State the preparation type.
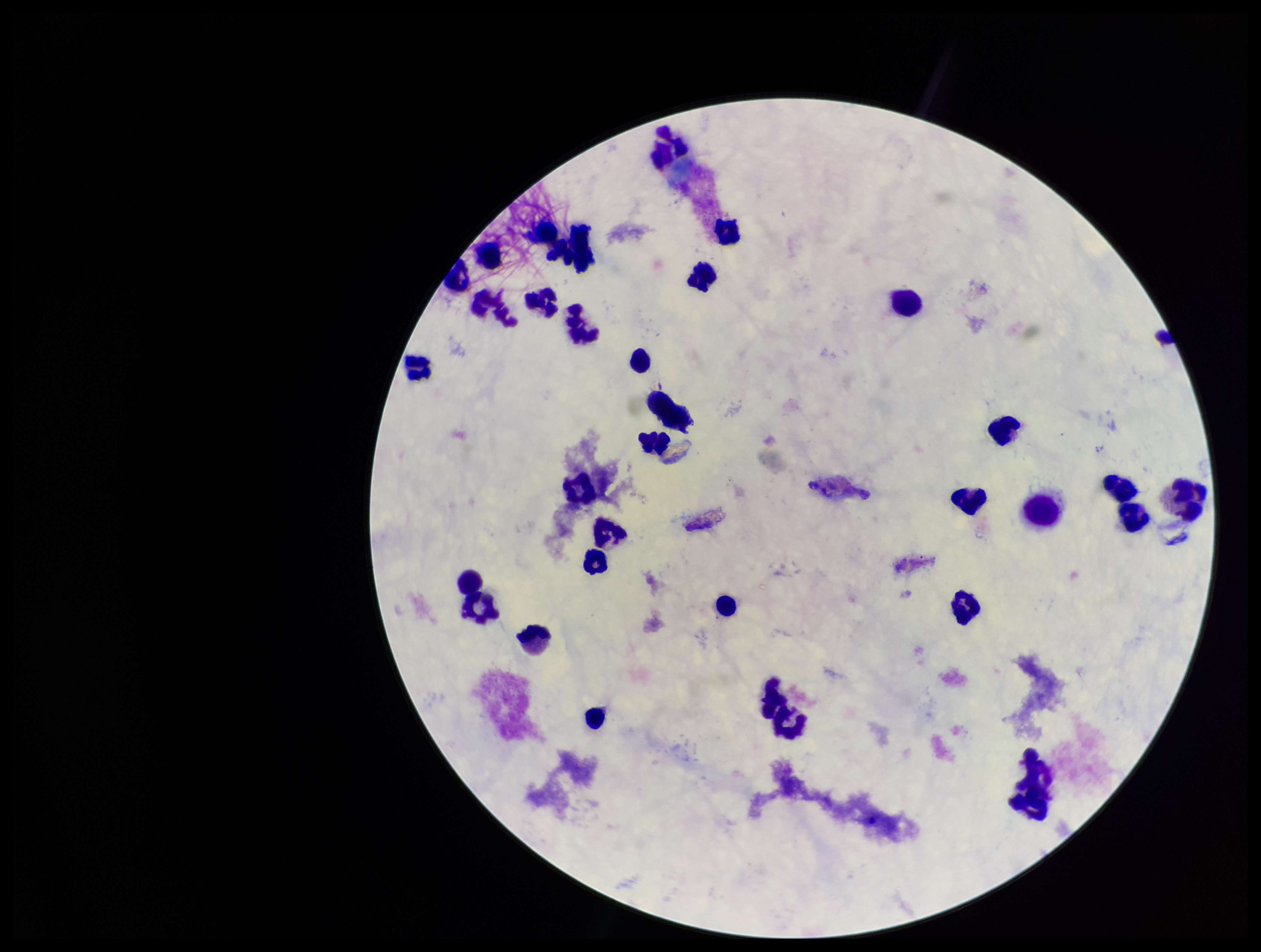
Thick.

Summary:
  - Plasmodium parasites: none seen
  - Patient malaria status: negative
  - Image size: 1261×952 pixels
  - Field of view: single
  - Parasite count: 0
  - Leukocyte count: 31
  - Stain: Giemsa
  - Capture: smartphone photograph through the microscope eyepiece